Name the parasite shown.
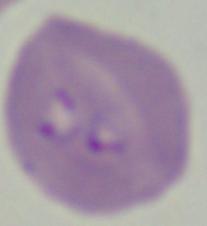
This is Babesia.

Summary:
  - Modality: micrograph
  - Magnification: 1000x